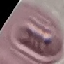
Result: no malaria parasites seen. Thin blood film. Giemsa-stained preparation. Acquired by smartphone through the microscope eyepiece. Cell patch, automatically extracted from a larger field of view and resized to 64 × 64 pixels.